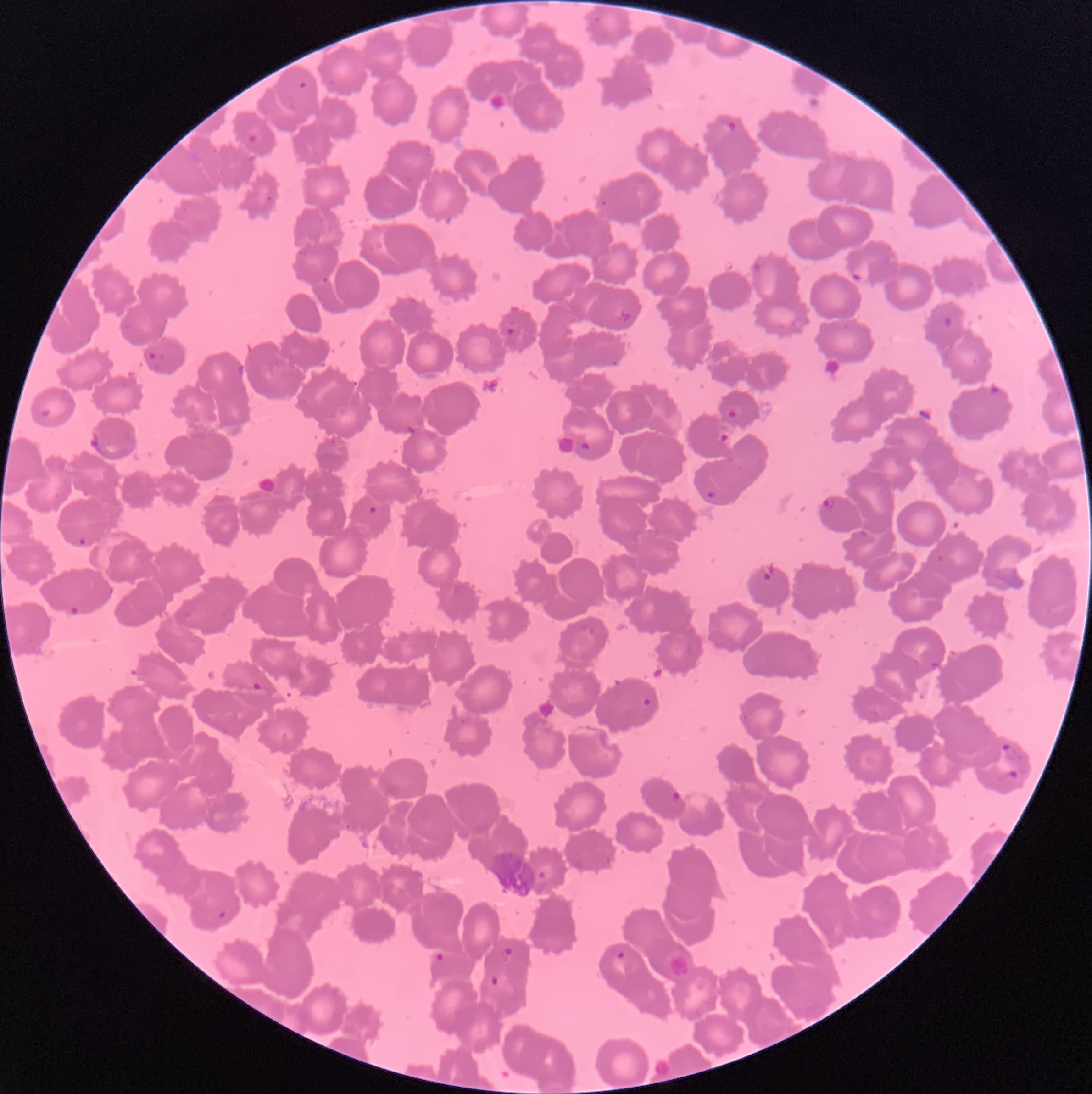
Summary:
  - Coordinate format: approximate bounding boxes as (x1,y1)-(x2,y2) corner pairs in pixels
  - Plasmodium parasites too small for a box (approximate centers as (x,y) in pixels): (269,198)
  - Plasmodium parasite locations: (299,80)-(308,90), (721,120)-(737,132), (247,132)-(258,144), (752,261)-(762,273), (850,268)-(863,283), (321,277)-(329,283), (617,309)-(631,323), (942,316)-(952,328), (507,327)-(515,335), (149,351)-(164,368), (238,364)-(244,375), (988,383)-(1001,397), (40,408)-(52,417), (727,409)-(738,419), (406,425)-(417,435), (90,431)-(101,448), (717,433)-(731,443), (580,441)-(590,450), (706,489)-(715,500), (822,495)-(836,512), (368,506)-(378,514), (858,529)-(869,537), (72,535)-(89,548), (937,554)-(944,563), (757,562)-(776,580), (70,605)-(82,616), (929,661)-(940,669), (252,682)-(264,691), (641,697)-(651,707), (1002,743)-(1023,763), (1007,769)-(1020,781), (671,791)-(682,802), (538,869)-(546,880), (217,910)-(227,920), (500,946)-(513,961), (616,951)-(626,960), (432,952)-(445,963), (490,976)-(501,987)
  - Preparation: thin blood film
  - Image size: 1092×1094 pixels
  - Red blood cell morphology: rouleaux formation
  - Modality: light microscopy